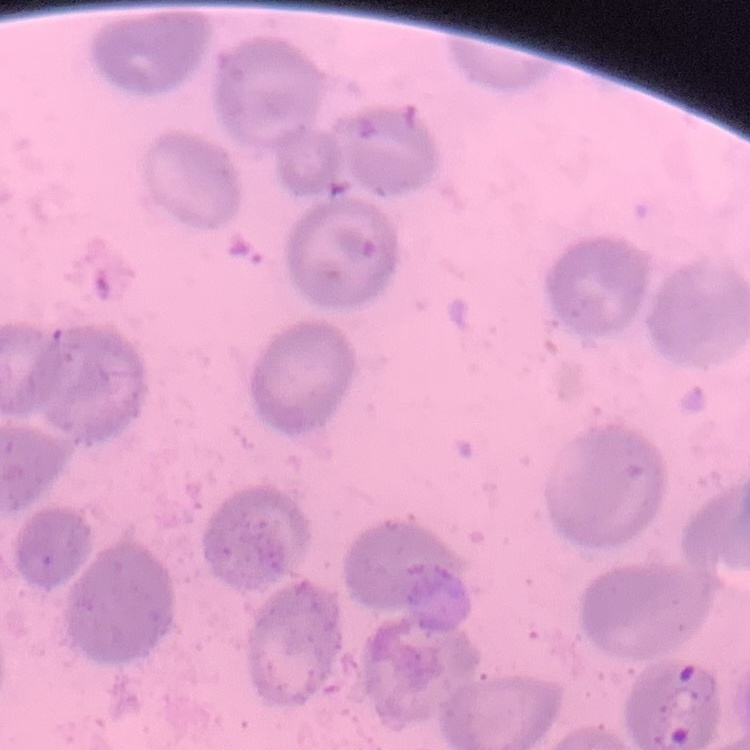 The erythrocytes exhibit no rouleaux formation. Thin peripheral smear. One tile cut from a larger photomicrograph. Field's or Giemsa stain.